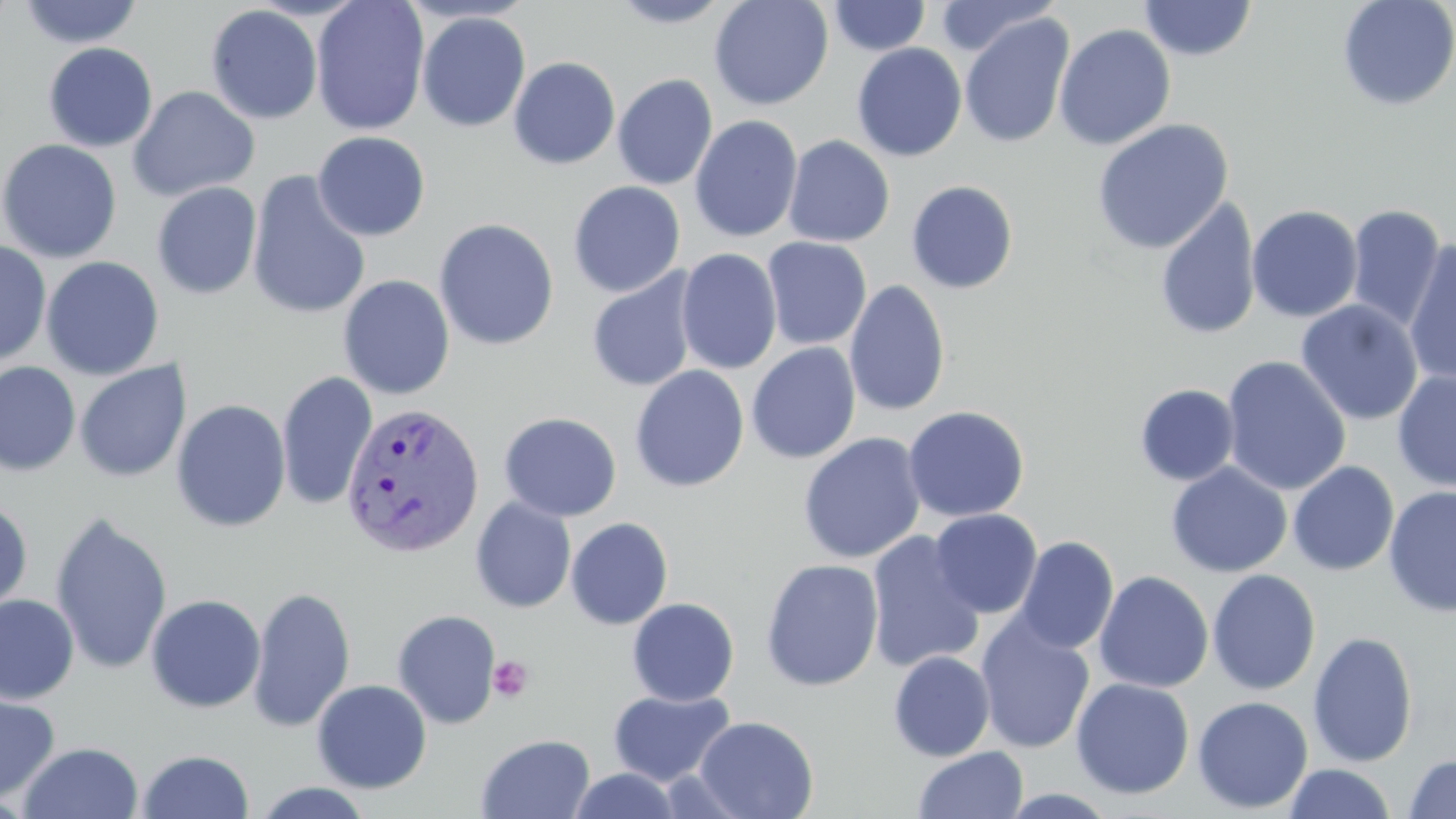

Approximate bounding boxes as (x1,y1)-(x2,y2) corner pairs in pixels. Platelet locations: (488,655)-(534,703). Uninfected red blood cell locations: (311,0)-(431,136), (608,0)-(736,28), (708,0)-(834,110), (937,0)-(1059,57), (1139,0)-(1257,61), (1337,0)-(1456,111), (18,1)-(143,49), (829,1)-(930,56), (206,4)-(323,124), (416,12)-(530,132), (959,13)-(1074,149), (1054,23)-(1176,151), (43,42)-(157,152), (851,42)-(967,161), (508,56)-(621,170), (612,74)-(718,190), (127,86)-(261,201), (689,115)-(803,243), (1092,118)-(1234,254), (312,131)-(431,241), (783,134)-(895,247), (0,138)-(123,264), (246,170)-(372,320), (568,180)-(685,298), (905,180)-(1019,294), (151,182)-(262,300), (1155,197)-(1261,341), (1246,204)-(1363,323), (1346,205)-(1448,331), (433,218)-(559,351), (762,237)-(872,350), (0,240)-(52,369), (1403,240)-(1456,387), (676,248)-(782,375), (41,256)-(164,380), (586,269)-(699,393), (338,274)-(455,400), (844,280)-(951,418), (1295,299)-(1424,426), (746,342)-(861,463), (1221,356)-(1351,496), (74,360)-(192,483), (0,361)-(81,476), (629,365)-(750,493), (1392,370)-(1456,492), (276,372)-(378,511), (1134,383)-(1240,486), (171,399)-(291,532), (903,405)-(1030,523), (498,411)-(622,522), (798,432)-(926,564), (1288,461)-(1399,576), (1166,462)-(1292,578), (1383,486)-(1456,618), (0,496)-(33,618), (470,497)-(576,614), (930,508)-(1043,619), (50,510)-(173,678), (565,517)-(673,629), (865,531)-(986,673), (1012,535)-(1119,655), (760,558)-(884,692), (1206,568)-(1321,695), (1094,570)-(1214,693), (247,585)-(356,733), (145,593)-(266,714), (0,594)-(79,705), (627,597)-(739,706), (392,609)-(501,728), (975,615)-(1095,753), (1307,631)-(1419,767), (888,651)-(995,762), (1070,678)-(1194,799), (312,679)-(432,793), (607,689)-(736,786), (1,690)-(60,805), (1192,695)-(1313,814), (694,715)-(819,819), (476,734)-(595,819), (18,741)-(144,819), (913,746)-(1028,819), (137,749)-(255,819), (1402,753)-(1456,819), (1283,762)-(1395,818), (567,769)-(682,819), (250,782)-(378,818), (997,789)-(1120,818). Plasmodium vivax-infected red blood cell locations: (340,401)-(485,559). Slide-level diagnosis: Plasmodium vivax. Captured at 1000x magnification. Light microscopy. Image is 1456×819 pixels. Thin blood smear. May-Grünwald-Giemsa-stained preparation. One field of a larger specimen.